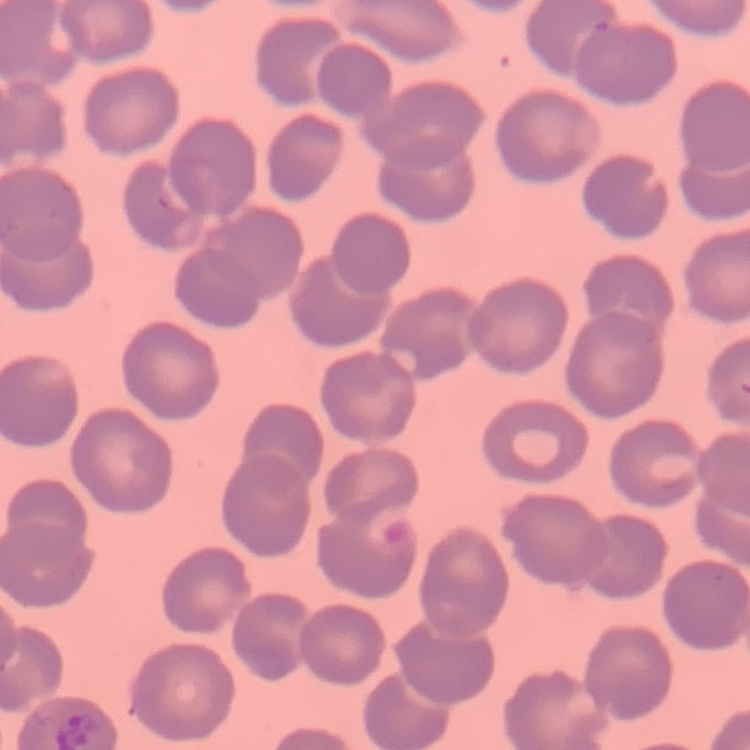
erythrocyte_morphology: no rouleaux formation
image_type: square crop of a larger photomicrograph
stain: Field's or Giemsa
preparation: thin blood smear